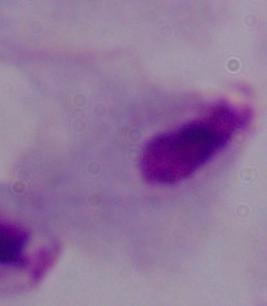

modality = photomicrograph
magnification = 1000x
identification = trichomonad